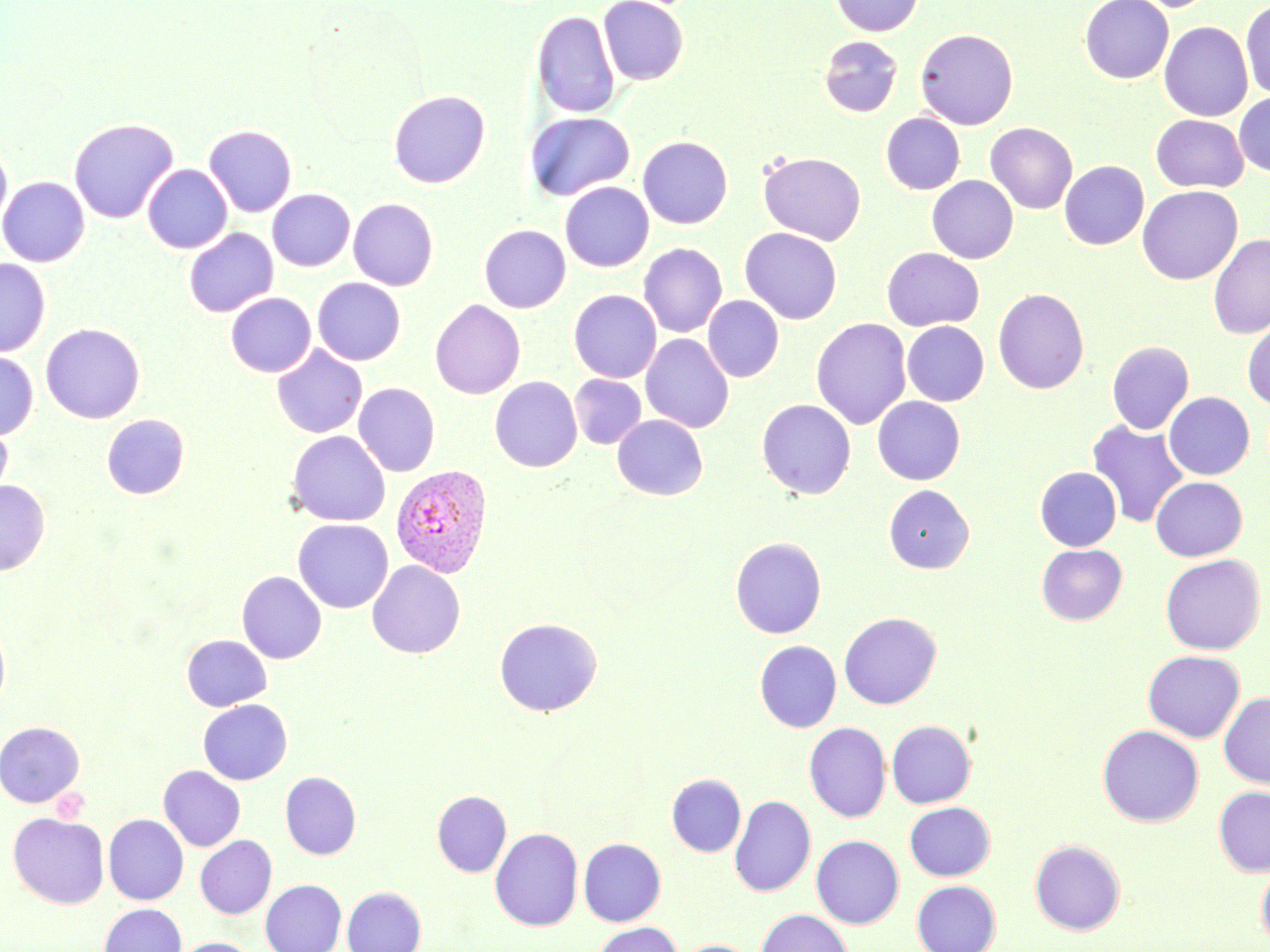
Approximate bounding boxes as [x1, y1, x2, y2] in pixels. Plasmodium vivax-infected red blood cell locations: [389, 464, 493, 578]. Uninfected red blood cell locations: [598, 0, 688, 85], [829, 0, 924, 37], [1079, 0, 1173, 83], [1119, 0, 1221, 12], [1240, 0, 1270, 100], [531, 10, 620, 119], [1159, 21, 1253, 122], [915, 28, 1018, 130], [818, 35, 903, 118], [387, 90, 491, 189], [1234, 92, 1270, 178], [524, 112, 635, 201], [881, 113, 965, 194], [1151, 114, 1248, 192], [68, 118, 179, 225], [985, 122, 1077, 214], [203, 124, 298, 217], [536, 131, 648, 257], [637, 136, 733, 229], [0, 140, 13, 230], [757, 151, 866, 245], [1059, 160, 1149, 250], [142, 164, 233, 254], [926, 175, 1019, 264], [0, 176, 90, 267], [560, 182, 654, 272], [1137, 185, 1242, 285], [267, 189, 355, 272], [348, 198, 439, 290], [479, 224, 571, 313], [183, 227, 278, 318], [739, 227, 843, 325], [1208, 235, 1270, 340], [638, 243, 728, 338], [882, 247, 984, 331], [0, 258, 51, 357], [312, 278, 406, 365], [992, 287, 1090, 394], [568, 290, 662, 383], [225, 292, 315, 377], [703, 295, 784, 382], [429, 299, 526, 399], [811, 318, 912, 430], [902, 320, 989, 406], [1242, 320, 1270, 409], [40, 322, 146, 424], [640, 333, 734, 434], [1106, 340, 1194, 435], [272, 345, 368, 438], [0, 350, 39, 441], [569, 374, 646, 449], [489, 376, 583, 473], [353, 382, 441, 477], [1164, 391, 1255, 480], [872, 396, 965, 485], [756, 399, 856, 499], [101, 414, 190, 499], [612, 414, 707, 500], [1087, 419, 1189, 528], [0, 420, 13, 507], [286, 430, 391, 526], [1034, 467, 1122, 551], [1150, 476, 1247, 561], [0, 480, 50, 576], [883, 484, 974, 574], [292, 519, 393, 613], [730, 536, 827, 638], [1036, 544, 1127, 625], [1159, 554, 1265, 654], [367, 560, 466, 658], [236, 570, 327, 664], [838, 611, 942, 709], [494, 617, 602, 716], [0, 618, 11, 715], [181, 634, 271, 711], [754, 639, 841, 732], [1142, 650, 1245, 742], [1219, 691, 1270, 788], [198, 699, 292, 785], [886, 719, 976, 808], [0, 720, 85, 808], [804, 722, 891, 822], [1097, 725, 1204, 827], [158, 765, 246, 852], [280, 771, 361, 859], [667, 773, 746, 857], [1213, 785, 1270, 877], [432, 790, 511, 877], [729, 795, 815, 897], [904, 802, 995, 880], [7, 811, 110, 909], [103, 814, 189, 905], [490, 827, 583, 931], [195, 835, 277, 919], [811, 835, 904, 929], [578, 838, 666, 926], [1030, 839, 1126, 935], [1256, 857, 1270, 950], [260, 879, 347, 952], [911, 880, 1001, 952], [342, 886, 426, 952], [98, 903, 187, 952], [756, 908, 854, 952], [593, 922, 682, 952], [172, 937, 258, 952], [678, 939, 757, 952]. Slide-level diagnosis: Plasmodium vivax. Single field of view. Optical microscopy. Thin blood smear. 1000x magnification. May-Grünwald-Giemsa stain. Image is 1270×952 pixels.